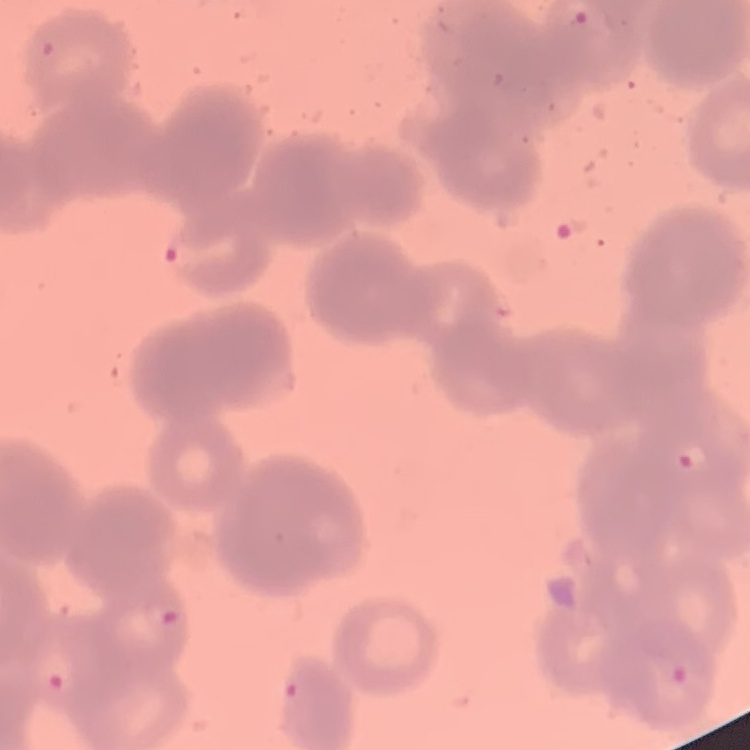

erythrocyte morphology = rouleaux formation
stain = Field's or Giemsa
preparation = thin blood smear
image type = one tile cut from a larger photomicrograph